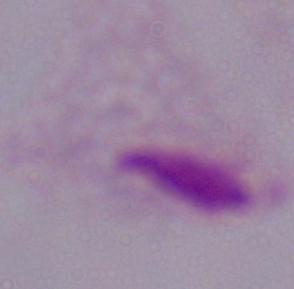 A trichomonad is shown. Captured at 1000x magnification. Micrograph.